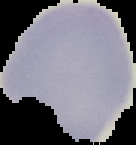
result = no malaria parasites seen
image size = 136×145 pixels
image type = cell region segmented out of the field of view; surrounding area masked to black
preparation = thin blood smear